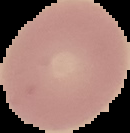
Summary:
  - Result: no Plasmodium parasites detected
  - Image size: 130×133 pixels
  - Image type: segmented cell region on a black background
  - Preparation: thin blood smear